State the preparation type.
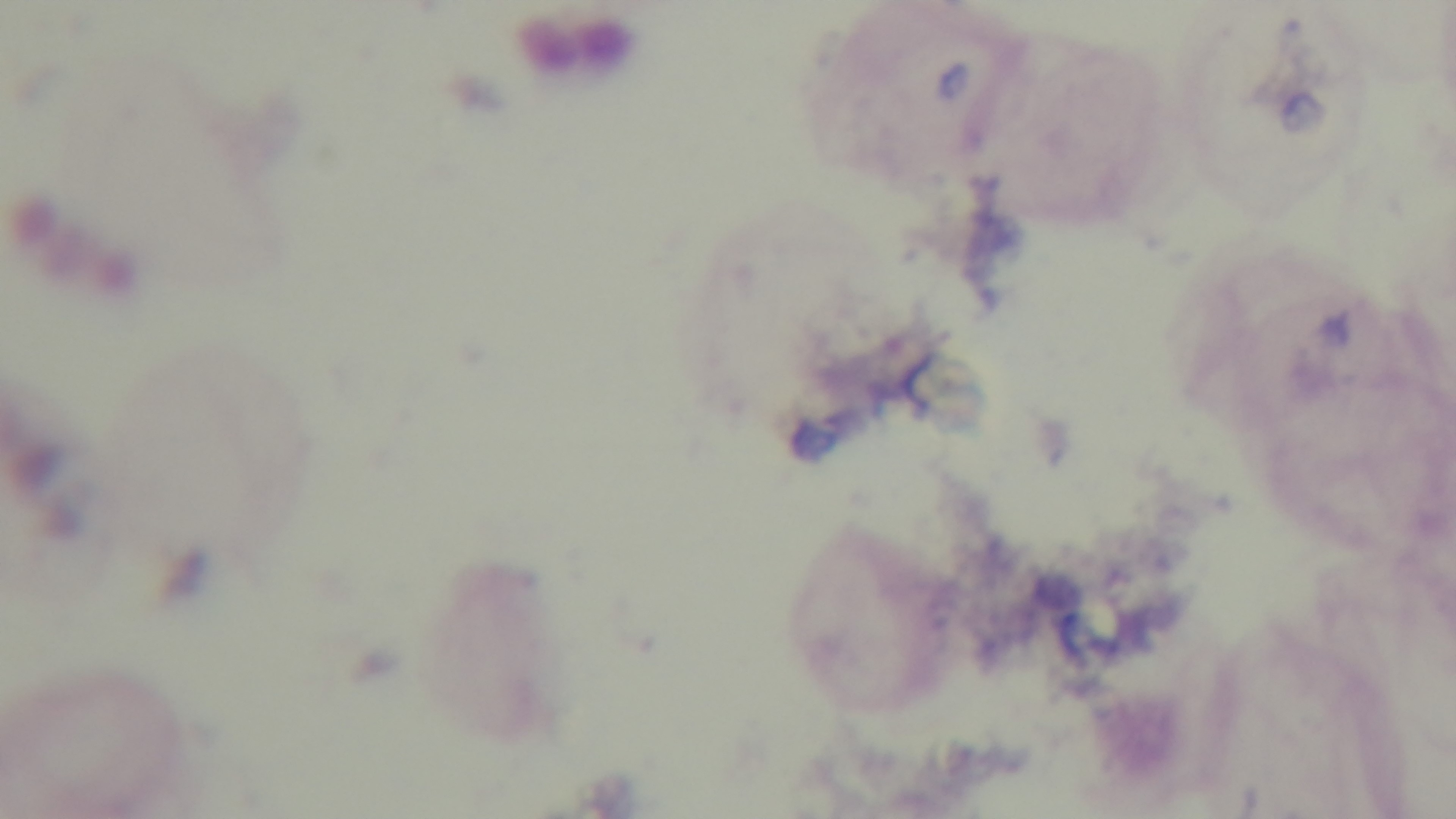

A thick smear.

capture = mounted 4K digital camera
stain = Giemsa
modality = light microscopy
objective = 100x oil immersion
malaria status = negative
field of view = single